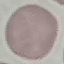
Summary:
  - Malaria status: uninfected
  - Preparation: thin blood film
  - Capture: smartphone through the microscope eyepiece
  - Image type: automatically extracted cell patch, resized to 64 × 64 pixels
  - Stain: Giemsa